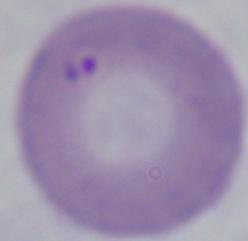

Photomicrograph. Captured at 1000x magnification. A Babesia parasite is seen.